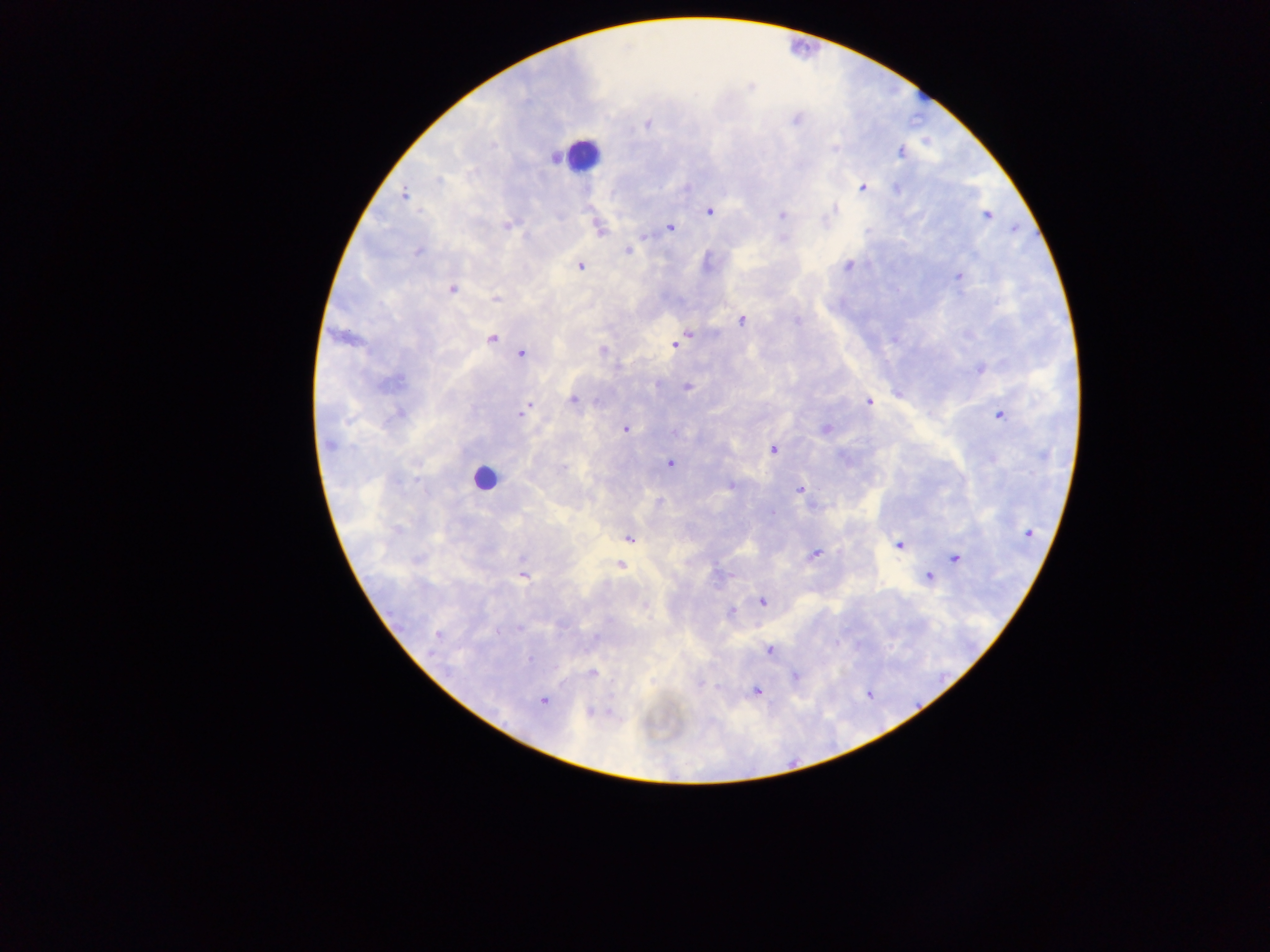

Plasmodium parasite locations = approximate centers as (x, y) in pixels: (795, 119), (647, 125), (900, 152), (439, 180), (863, 187), (897, 188), (404, 194), (835, 209), (709, 211), (781, 215), (987, 215), (507, 225), (670, 227), (599, 230), (628, 251), (418, 252), (848, 266), (581, 267), (958, 276), (451, 289), (495, 299), (798, 320), (742, 321), (687, 335), (491, 339), (676, 343), (603, 350), (522, 353), (980, 368), (395, 382), (687, 388), (573, 400), (869, 401), (526, 408), (521, 413), (398, 414), (999, 415), (625, 429), (826, 429), (329, 444), (773, 449), (670, 463), (731, 486), (799, 489), (773, 513), (1028, 533), (630, 538), (900, 545), (814, 554), (956, 558), (620, 565), (523, 576), (928, 577), (762, 601), (644, 605), (731, 612), (520, 628), (497, 633), (438, 635), (595, 636), (768, 650), (529, 658), (591, 673), (795, 676), (757, 690), (543, 700), (590, 712)
leukocyte locations = approximate centers as (x, y) in pixels (subset; some below the resolvable size): (802, 45), (922, 93), (582, 155), (484, 478)
capture = mobile-phone photograph through a microscope
image size = 1270×952 pixels
preparation = thick blood smear
field of view = single
country = Ghana